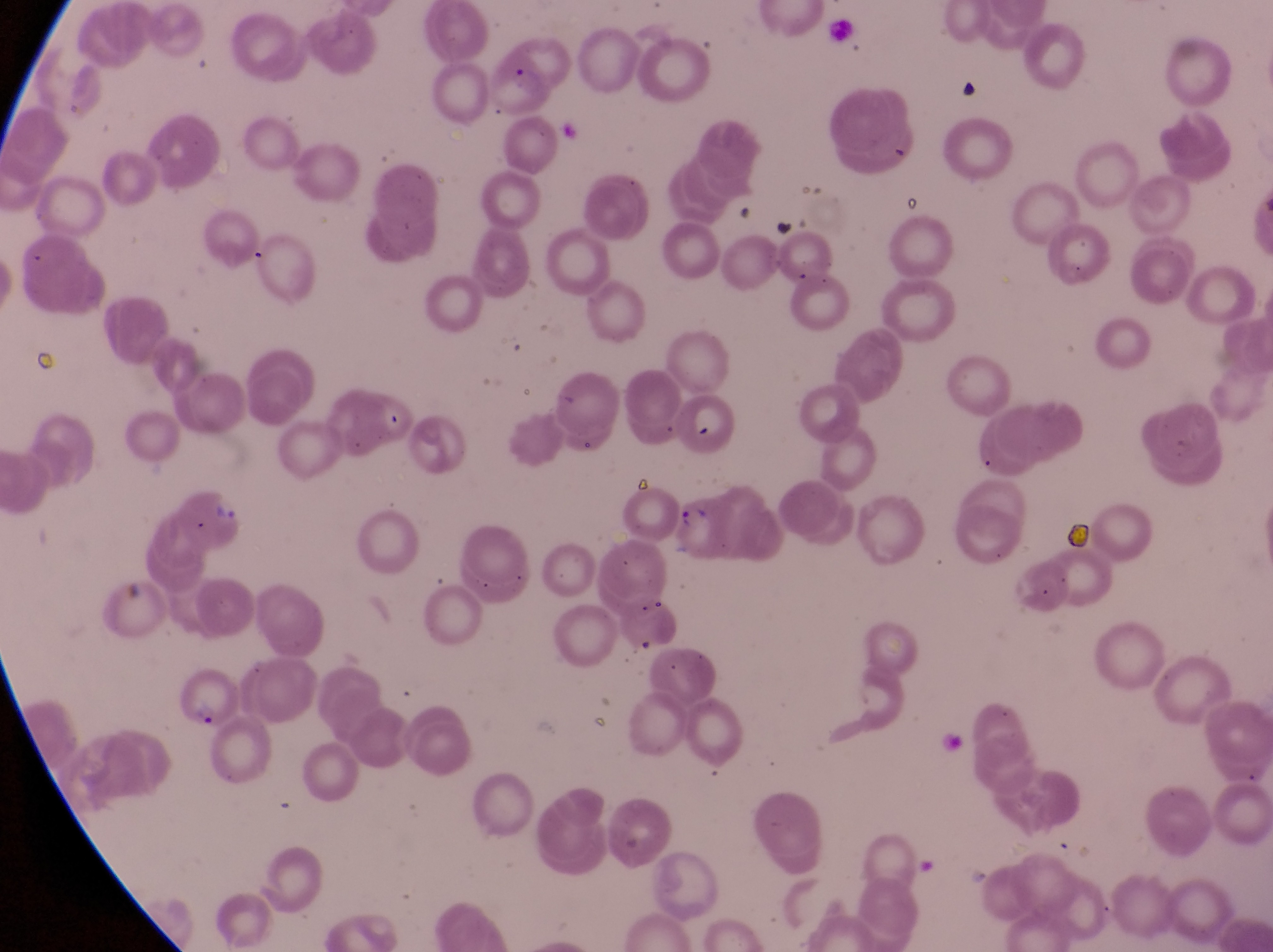
artifact (platelet-like body, stain precipitate, or debris) locations = approximate bounding boxes as [left, top, right, bottom] in pixels: [958, 68, 983, 105], [766, 207, 803, 246]
field of view = single
capture = smartphone photograph through the eyepiece of an Olympus CX-23 microscope
image size = 1273×952 pixels
country = Uganda
preparation = thin blood film
magnification = 1000x
parasitised red blood cell locations = approximate bounding boxes as [left, top, right, bottom] in pixels: [484, 42, 553, 116], [174, 484, 248, 546], [177, 669, 232, 734]